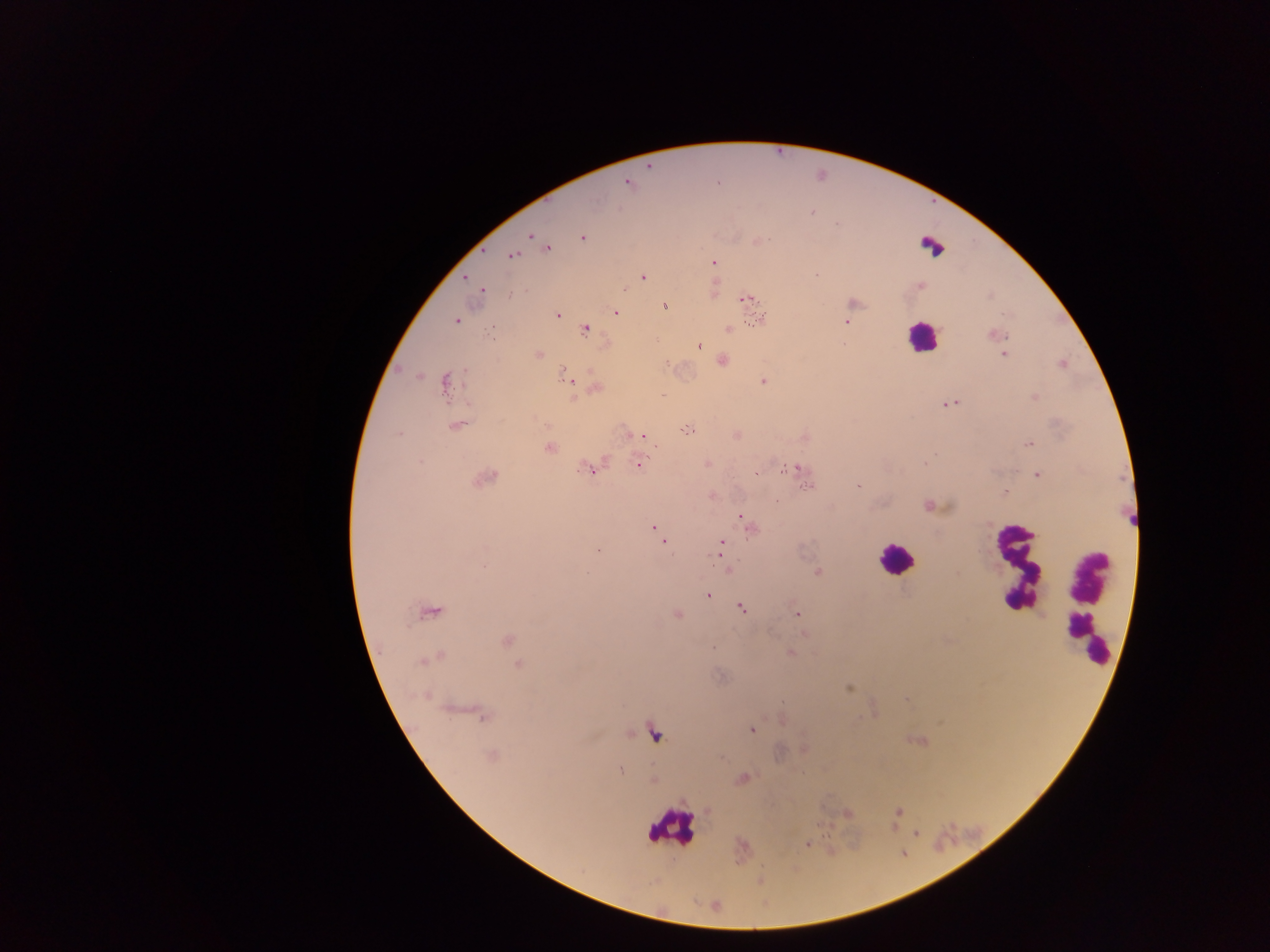
Approximate centers as (x, y) in pixels. Plasmodium parasite locations: (648, 164), (628, 182), (529, 236), (582, 237), (543, 243), (546, 248), (510, 254), (713, 263), (643, 276), (465, 277), (919, 285), (481, 289), (745, 298), (853, 303), (664, 306), (615, 312), (557, 314), (759, 318), (455, 320), (847, 322), (727, 327), (584, 329), (995, 335), (699, 345), (846, 345), (1004, 354), (538, 355), (721, 361), (1061, 363), (567, 377), (763, 381), (445, 383), (595, 388), (662, 395), (1035, 397), (949, 403), (456, 425), (689, 429), (736, 434), (641, 435), (1030, 443), (550, 447), (637, 463), (708, 463), (926, 463), (585, 468), (795, 468), (1037, 474), (485, 477), (809, 485), (859, 486), (1004, 491), (711, 495), (930, 505), (741, 517), (745, 521), (654, 528), (750, 528), (659, 536), (663, 542), (721, 547), (598, 550), (484, 566), (726, 568), (817, 572), (708, 596), (742, 607), (429, 610), (677, 614), (797, 614), (804, 633), (506, 640), (790, 652), (431, 658), (519, 665), (848, 688), (483, 715), (750, 729), (654, 732), (918, 741), (491, 755), (620, 770), (743, 778), (652, 780), (899, 811), (845, 814), (807, 844). Leukocyte locations: (922, 337), (896, 560), (1016, 567), (1087, 609), (670, 827). Thick blood smear. Photographed through a microscope with a mobile-phone camera. Image is 1270×952 pixels. One field of view. Collected in Ghana.